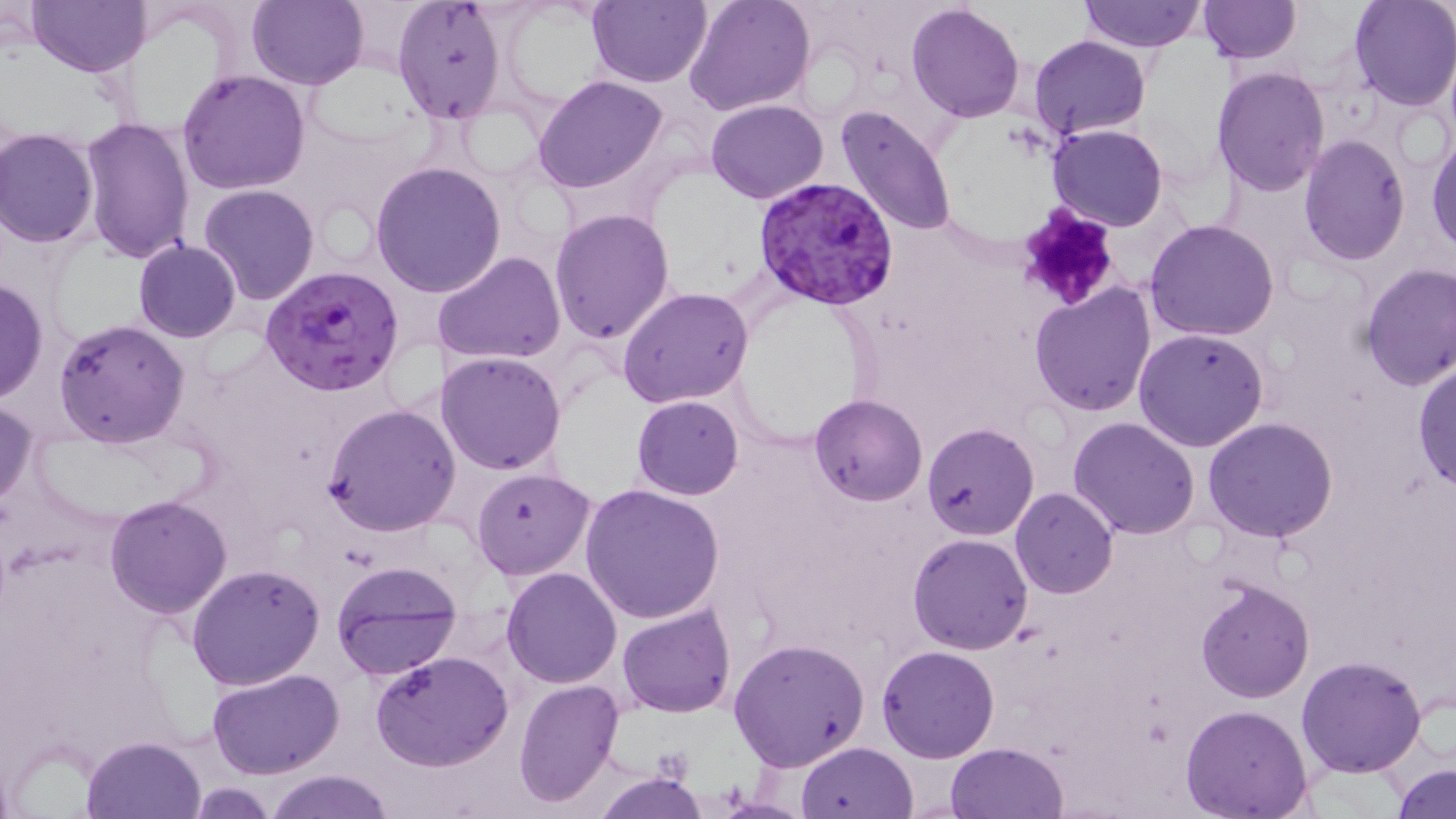
Approximate bounding boxes as (x1,y1)-(x2,y2) corner pairs in pixels. Plasmodium falciparum-infected red blood cell locations: (753,175)-(898,313), (260,264)-(406,397). Uninfected red blood cell locations: (27,0)-(151,76), (246,0)-(369,89), (586,0)-(711,87), (685,0)-(816,117), (1079,0)-(1204,52), (1197,1)-(1302,65), (1347,1)-(1455,111), (905,2)-(1026,123), (391,3)-(505,124), (1029,35)-(1150,139), (1210,65)-(1329,196), (176,68)-(311,194), (533,74)-(670,194), (706,99)-(829,203), (835,104)-(958,238), (81,116)-(195,263), (1046,122)-(1168,233), (0,129)-(100,247), (1427,129)-(1456,256), (1298,134)-(1410,263), (369,161)-(507,299), (198,184)-(322,305), (549,207)-(676,344), (1145,218)-(1280,340), (134,240)-(242,342), (435,251)-(566,366), (1358,262)-(1456,389), (0,277)-(48,406), (1029,282)-(1157,416), (617,287)-(754,409), (54,318)-(190,448), (1133,328)-(1270,452), (436,351)-(566,476), (1412,355)-(1456,489), (809,393)-(928,507), (632,396)-(744,499), (1,402)-(38,512), (322,404)-(462,535), (1069,416)-(1200,539), (1202,417)-(1337,541), (923,423)-(1039,540), (471,467)-(594,579), (580,483)-(725,623), (1010,488)-(1117,598), (103,494)-(232,618), (908,533)-(1033,654), (329,559)-(467,684), (185,562)-(325,689), (502,568)-(621,688), (1195,578)-(1314,703), (617,604)-(736,718), (729,636)-(872,775), (878,645)-(1000,762), (371,651)-(515,770), (1296,654)-(1428,776), (209,667)-(345,779), (515,678)-(625,807), (1179,703)-(1315,819), (82,735)-(205,818), (797,741)-(918,819), (947,742)-(1068,819), (1392,764)-(1455,819), (592,768)-(708,819), (265,769)-(396,819), (187,783)-(275,816). Platelet locations: (1013,205)-(1122,314). Slide-level diagnosis: Plasmodium falciparum. Thin blood smear. Single field of view. Light microscopy. May-Grünwald-Giemsa-stained preparation. Image is 1456×819 pixels. 1000x magnification.